Outline each blood parasite and name the species.
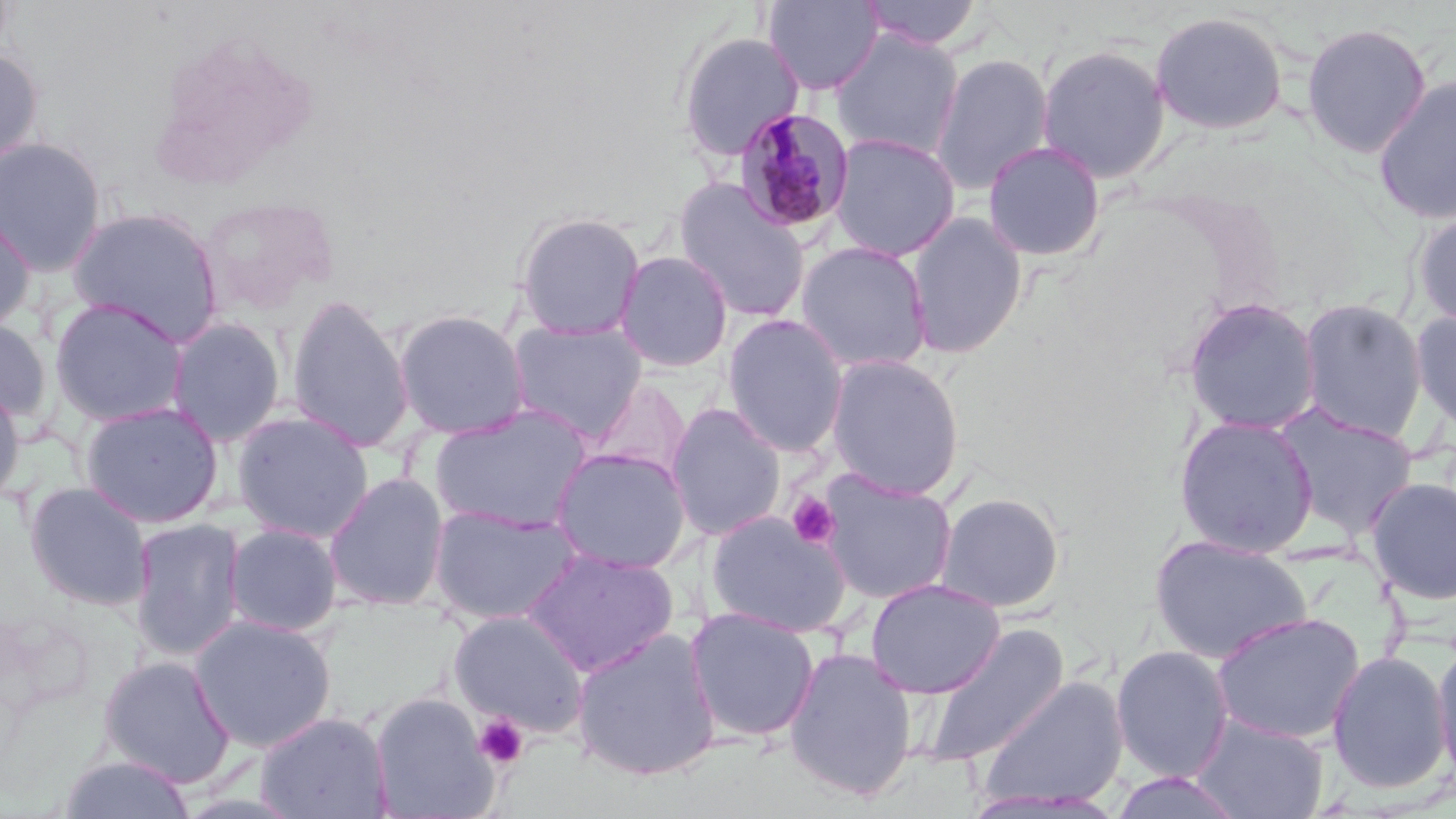

Approximate bounding boxes as (x1,y1)-(x2,y2) corner pairs in pixels.
Plasmodium malariae-infected red blood cells: (732,108)-(856,233).
No Plasmodium falciparum, Plasmodium ovale, Plasmodium vivax, Babesia divergens, or Trypanosoma brucei observed.

slide-level diagnosis = Plasmodium malariae
platelet locations = approximate bounding boxes as (x1,y1)-(x2,y2) corner pairs in pixels: (787,492)-(839,549), (474,713)-(528,769)
image size = 1456×819 pixels
magnification = 1000x
field of view = one of a larger specimen
modality = light microscopy
uninfected red blood cell locations = approximate bounding boxes as (x1,y1)-(x2,y2) corner pairs in pixels: (761,0)-(885,95), (859,0)-(985,51), (1149,10)-(1289,136), (1300,21)-(1432,159), (830,30)-(964,161), (674,31)-(805,162), (1036,44)-(1171,184), (0,46)-(44,169), (929,51)-(1054,195), (1373,75)-(1456,225), (828,132)-(961,262), (0,137)-(108,276), (982,140)-(1106,263), (672,176)-(812,323), (197,195)-(337,317), (66,206)-(226,346), (1410,208)-(1456,331), (0,209)-(36,336), (513,211)-(647,341), (904,211)-(1029,359), (795,241)-(933,373), (614,250)-(734,373), (285,293)-(415,453), (1182,296)-(1322,436), (49,297)-(190,427), (1296,297)-(1429,443), (1410,307)-(1456,433), (393,308)-(531,440), (721,313)-(850,457), (0,316)-(54,427), (165,317)-(286,447), (506,318)-(647,442), (825,354)-(966,499), (585,378)-(693,483), (0,382)-(26,508), (79,401)-(224,528), (665,403)-(786,541), (1275,404)-(1419,540), (429,405)-(593,532), (233,410)-(374,543), (1173,414)-(1319,558), (549,446)-(693,574), (818,470)-(958,605), (323,472)-(450,611), (1365,476)-(1456,604), (24,480)-(154,611), (935,492)-(1066,613), (429,504)-(584,626), (706,509)-(851,637), (129,518)-(246,662), (224,524)-(342,637), (1149,533)-(1312,664), (522,548)-(678,677), (865,578)-(1005,698), (684,606)-(820,743), (448,610)-(589,736), (1211,612)-(1365,744), (190,614)-(337,752), (917,623)-(1070,768), (570,626)-(722,781), (1431,637)-(1456,785), (1110,644)-(1234,782), (784,646)-(919,802), (1326,649)-(1451,794), (97,654)-(236,788), (975,675)-(1128,812), (369,692)-(499,819), (254,710)-(392,819), (1191,713)-(1328,819), (57,753)-(197,818), (1110,771)-(1245,818)
stain = May-Grünwald-Giemsa
preparation = thin blood smear